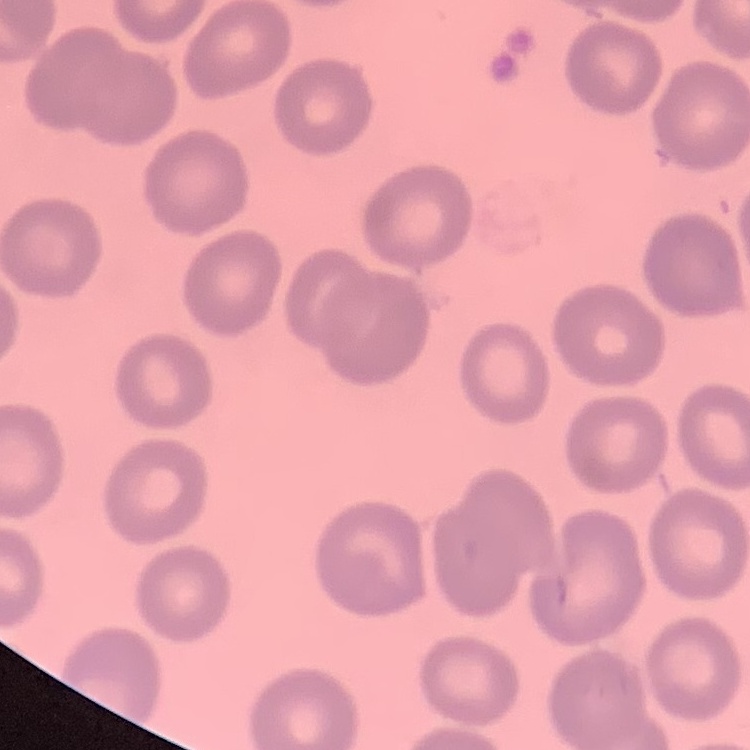

Summary:
  - Red blood cell morphology: no rouleaux formation
  - Stain: Field's or Giemsa
  - Image type: square crop of a larger photomicrograph
  - Preparation: thin peripheral smear